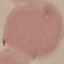
malaria status = uninfected
preparation = thin blood film
image type = automatically extracted cell patch, resized to 64 × 64 pixels
stain = Giemsa
capture = smartphone through the microscope eyepiece